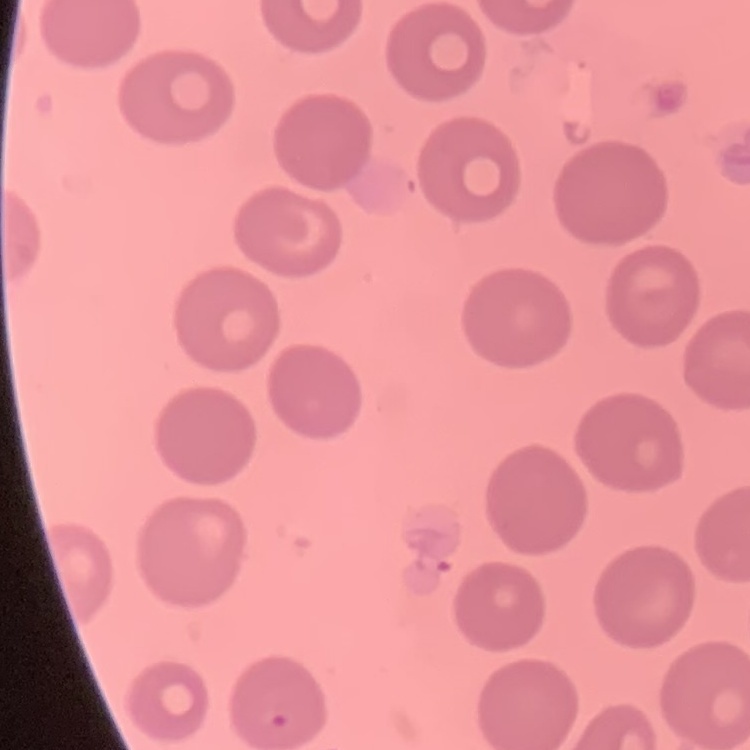

red blood cell morphology = no rouleaux formation
image type = square crop of a larger photomicrograph
preparation = thin blood smear
stain = Field's or Giemsa